Give the position of every leukocyte visible.
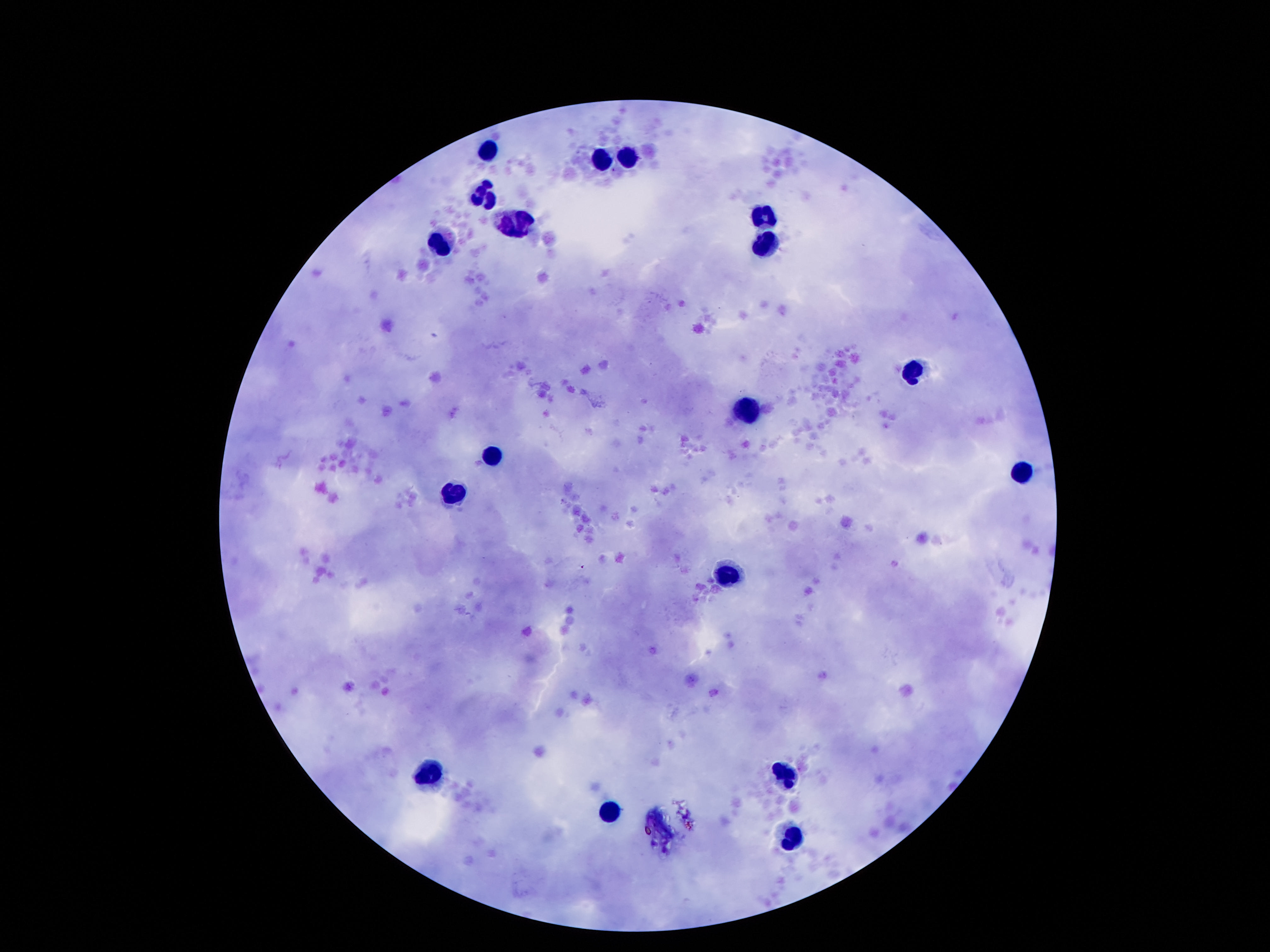

Approximate centers as (x, y) in pixels.
Leukocytes: (488, 149), (630, 153), (598, 159), (484, 189), (768, 213), (512, 227), (760, 245), (442, 247), (912, 373), (746, 405), (492, 457), (1020, 473), (452, 493), (724, 565), (433, 773), (786, 777), (610, 809), (790, 833).

preparation = thick peripheral-blood smear
image size = 1270×952 pixels
capture = smartphone camera through the microscope eyepiece
stain = Giemsa
patient malaria status = not infected
magnification = 100x
field of view = one from this slide